Comment on the morphology of the erythrocytes.
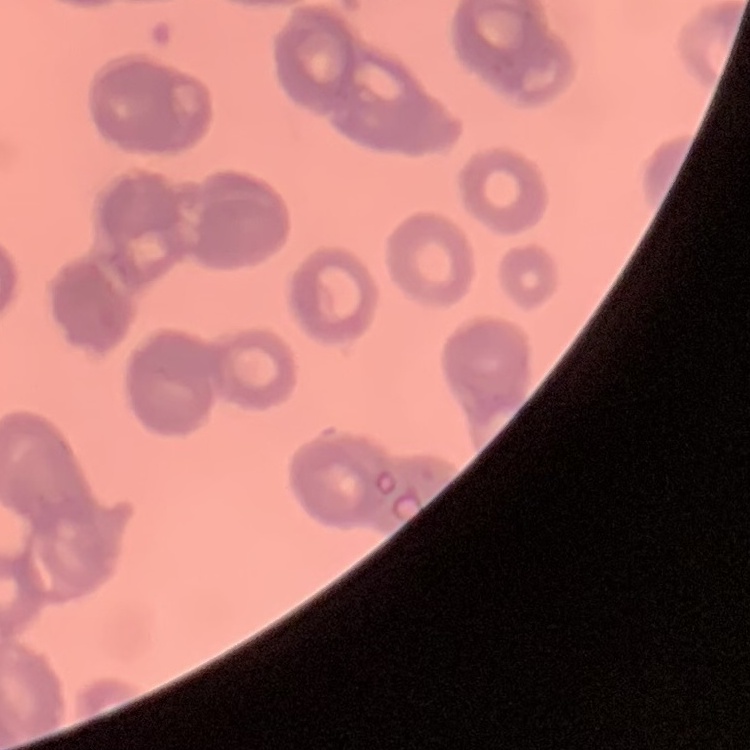
They show rouleaux formation.

One tile cut from a larger photomicrograph. Field's or Giemsa stain. Thin blood film.